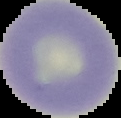
preparation = thin blood film
result = no malaria parasites seen
image type = cell region segmented out of the field of view; surrounding area masked to black
image size = 121×118 pixels